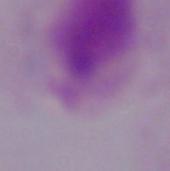

Micrograph. 1000x magnification. A trichomonad is seen.